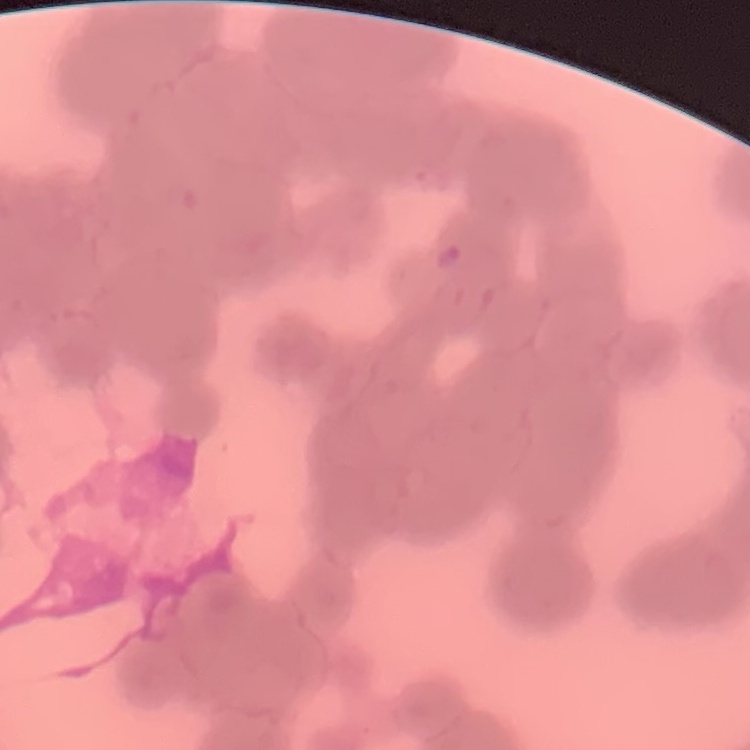

The red blood cells exhibit rouleaux formation. Stained with either Field's or Giemsa. Square crop of a larger photomicrograph. Thin blood smear.